Assess this cell for malaria.
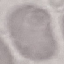
Uninfected.

stain = Giemsa
capture = smartphone camera at the microscope eyepiece
image type = automatically extracted cell patch, resized to 64 × 64 pixels
preparation = thin blood smear